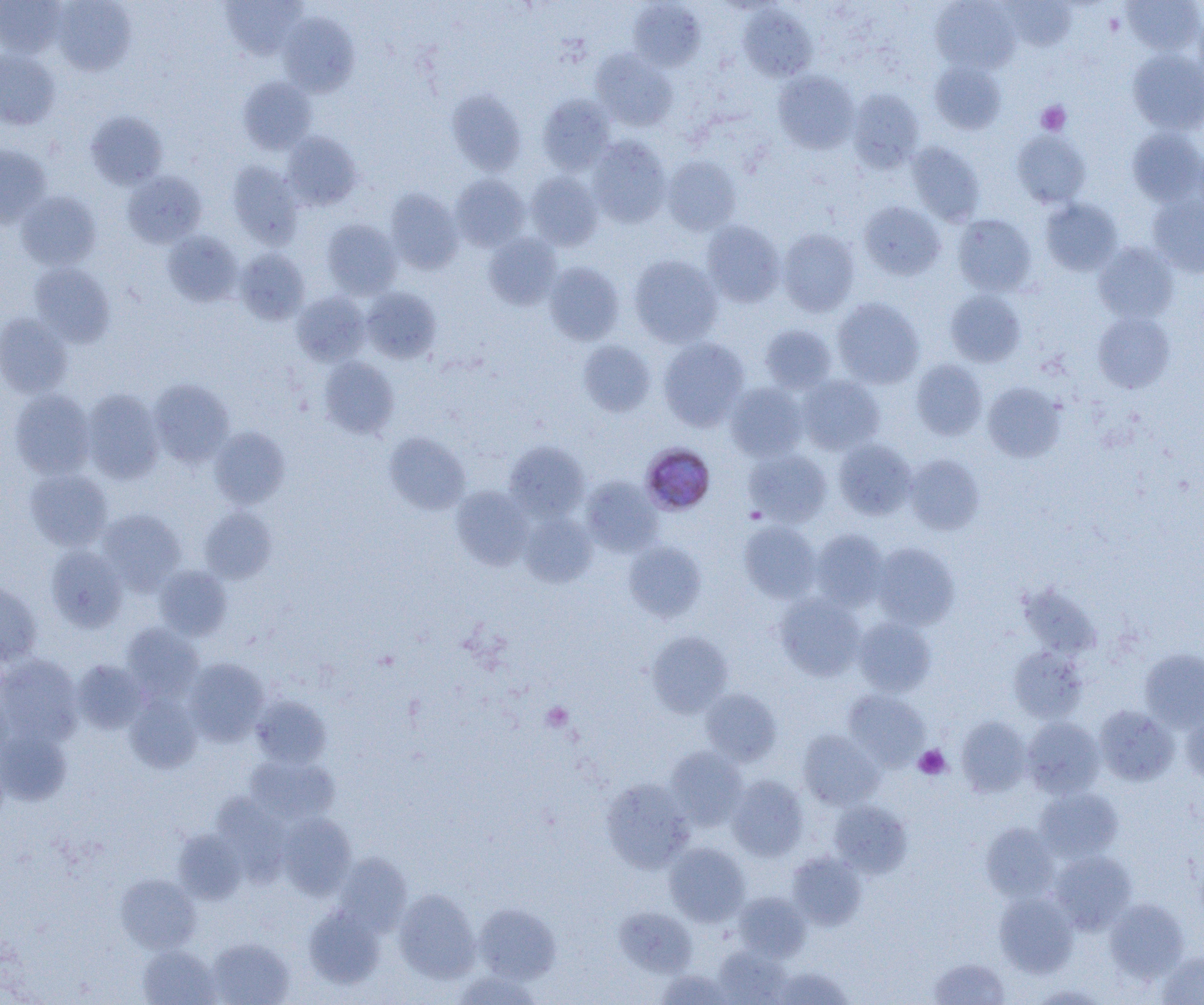
slide_level_diagnosis: Plasmodium malariae
image_size: 1204×1005 pixels
magnification: 1000x
preparation: thin blood smear
platelet_locations: 'approximate bounding boxes as [x1, y1, x2, y2] in pixels: [1036, 101, 1071, 135], [542, 702, 574, 731], [914, 745, 951, 780]'
modality: light microscopy
uninfected_red_blood_cell_locations: 'approximate bounding boxes as [x1, y1, x2, y2] in pixels: [0, 0, 65, 58], [52, 0, 136, 75], [219, 0, 306, 60], [930, 0, 1020, 73], [1002, 0, 1075, 51], [1122, 0, 1203, 56], [628, 1, 705, 70], [738, 4, 816, 81], [279, 13, 359, 97], [1193, 13, 1204, 87], [1128, 49, 1204, 135], [0, 50, 60, 130], [590, 50, 677, 130], [930, 61, 1006, 134], [773, 71, 859, 154], [238, 77, 316, 154], [446, 89, 526, 175], [848, 89, 924, 172], [537, 94, 616, 174], [86, 110, 168, 190], [1127, 127, 1204, 207], [1011, 130, 1091, 209], [281, 132, 362, 210], [587, 136, 671, 227], [906, 142, 985, 225], [0, 144, 51, 228], [663, 156, 741, 235], [228, 162, 303, 248], [122, 171, 207, 249], [526, 171, 603, 250], [450, 174, 530, 251], [385, 188, 463, 274], [16, 191, 100, 270], [1147, 194, 1204, 278], [1041, 198, 1122, 276], [858, 201, 945, 280], [953, 214, 1036, 296], [321, 219, 401, 299], [701, 220, 784, 306], [777, 228, 859, 316], [163, 231, 242, 307], [484, 233, 562, 309], [1093, 241, 1179, 323], [234, 249, 310, 325], [629, 255, 723, 347], [30, 262, 115, 348], [544, 262, 624, 345], [361, 287, 441, 363], [946, 290, 1026, 366], [292, 292, 369, 366], [832, 298, 924, 388], [1092, 311, 1176, 393], [0, 313, 73, 398], [759, 324, 836, 394], [658, 338, 749, 431], [578, 340, 656, 416], [319, 357, 399, 438], [911, 359, 987, 440], [798, 375, 884, 455], [149, 379, 233, 466], [983, 382, 1065, 462], [725, 383, 808, 461], [9, 389, 95, 478], [81, 389, 165, 484], [209, 427, 290, 508], [384, 432, 470, 515], [834, 438, 916, 519], [504, 441, 589, 521], [744, 449, 831, 526], [904, 454, 985, 535], [24, 468, 113, 550], [581, 476, 663, 557], [451, 486, 533, 570], [199, 506, 276, 583], [97, 509, 186, 593], [519, 512, 598, 587], [740, 521, 821, 602], [811, 529, 888, 610], [623, 540, 706, 622], [871, 542, 959, 629], [46, 545, 127, 631], [154, 565, 232, 639], [0, 582, 42, 665], [1018, 583, 1102, 659], [776, 594, 866, 681], [853, 617, 936, 696], [121, 623, 204, 701], [646, 631, 733, 716], [1009, 647, 1088, 722], [1140, 649, 1204, 731], [0, 655, 83, 746], [185, 658, 269, 745], [72, 660, 148, 734], [701, 688, 781, 765], [844, 690, 930, 769], [125, 692, 202, 773], [252, 696, 330, 768], [1094, 706, 1179, 785], [1181, 708, 1204, 783], [956, 716, 1031, 797], [1022, 717, 1105, 798], [0, 727, 71, 805], [798, 730, 883, 811], [665, 746, 748, 830], [244, 754, 339, 826], [726, 776, 808, 861], [602, 779, 695, 872], [1034, 787, 1123, 863], [214, 794, 289, 885], [829, 800, 912, 877], [277, 813, 356, 899], [982, 823, 1060, 902], [174, 830, 247, 904], [665, 842, 750, 926], [1049, 850, 1136, 934], [787, 852, 866, 929], [335, 855, 411, 936], [116, 874, 199, 952], [393, 889, 481, 983], [734, 892, 811, 961], [995, 892, 1078, 978], [1105, 898, 1187, 981], [475, 903, 561, 984], [304, 905, 385, 989], [615, 907, 697, 976], [207, 937, 294, 1005], [138, 945, 221, 1005], [713, 945, 790, 1004], [1157, 950, 1204, 1004], [929, 957, 1009, 1004], [772, 966, 853, 1005], [452, 970, 541, 1005], [656, 970, 733, 1005]'
field_of_view: single
plasmodium_malariae_infected_red_blood_cell_locations: 'approximate bounding boxes as [x1, y1, x2, y2] in pixels: [640, 443, 715, 515]'